State the blood parasite species.
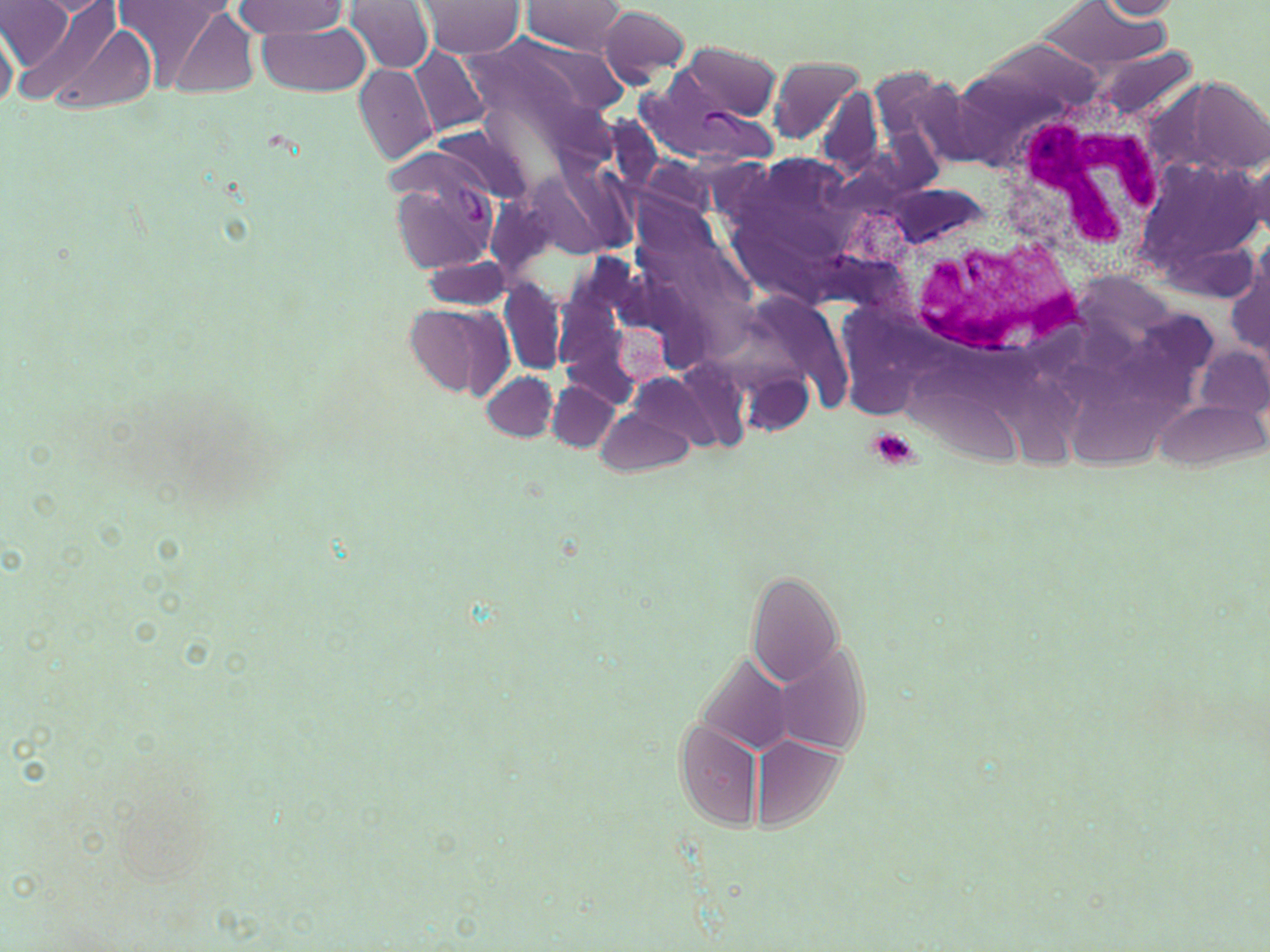
Plasmodium vivax.

Summary:
  - Coordinate format: approximate bounding boxes as named x1/y1/x2/y2 corners in pixels
  - Platelet locations: (x1=865, y1=429, x2=923, y2=469)
  - Plasmodium vivax-infected red blood cell locations: (x1=644, y1=58, x2=774, y2=154), (x1=387, y1=149, x2=506, y2=276)
  - White blood cell locations: (x1=1001, y1=91, x2=1172, y2=281), (x1=889, y1=203, x2=1097, y2=363)
  - Uninfected red blood cell locations: (x1=1, y1=0, x2=75, y2=72), (x1=112, y1=0, x2=232, y2=90), (x1=520, y1=0, x2=628, y2=55), (x1=1092, y1=0, x2=1182, y2=19), (x1=343, y1=1, x2=437, y2=74), (x1=15, y1=2, x2=125, y2=106), (x1=233, y1=2, x2=348, y2=38), (x1=416, y1=2, x2=525, y2=57), (x1=1032, y1=2, x2=1174, y2=72), (x1=162, y1=4, x2=261, y2=100), (x1=597, y1=6, x2=691, y2=85), (x1=0, y1=21, x2=18, y2=112), (x1=254, y1=21, x2=371, y2=97), (x1=473, y1=29, x2=631, y2=128), (x1=676, y1=43, x2=781, y2=120), (x1=1094, y1=46, x2=1197, y2=124), (x1=411, y1=47, x2=490, y2=136), (x1=766, y1=55, x2=866, y2=143), (x1=354, y1=64, x2=438, y2=165), (x1=867, y1=67, x2=967, y2=163), (x1=1174, y1=74, x2=1270, y2=179), (x1=817, y1=89, x2=884, y2=179), (x1=598, y1=117, x2=662, y2=191), (x1=1133, y1=152, x2=1262, y2=293), (x1=1239, y1=157, x2=1269, y2=241), (x1=528, y1=166, x2=629, y2=259), (x1=421, y1=254, x2=514, y2=312), (x1=1226, y1=254, x2=1269, y2=360), (x1=500, y1=280, x2=569, y2=376), (x1=406, y1=302, x2=514, y2=402), (x1=1196, y1=346, x2=1269, y2=422), (x1=739, y1=369, x2=814, y2=436), (x1=481, y1=370, x2=558, y2=441), (x1=548, y1=381, x2=621, y2=449), (x1=1153, y1=398, x2=1264, y2=471), (x1=597, y1=407, x2=693, y2=475), (x1=745, y1=570, x2=843, y2=688), (x1=772, y1=641, x2=871, y2=756), (x1=694, y1=653, x2=797, y2=754), (x1=675, y1=722, x2=763, y2=830), (x1=750, y1=737, x2=845, y2=828)
  - Magnification: 1000x
  - Image size: 1270×952 pixels
  - Preparation: thin blood film
  - Stain: May-Grünwald-Giemsa
  - Modality: optical microscopy
  - Field of view: single